Report the malaria status of this cell.
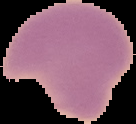

Parasitized.

Summary:
  - Image type: segmented cell region on a black background
  - Preparation: thin blood film
  - Image size: 136×124 pixels